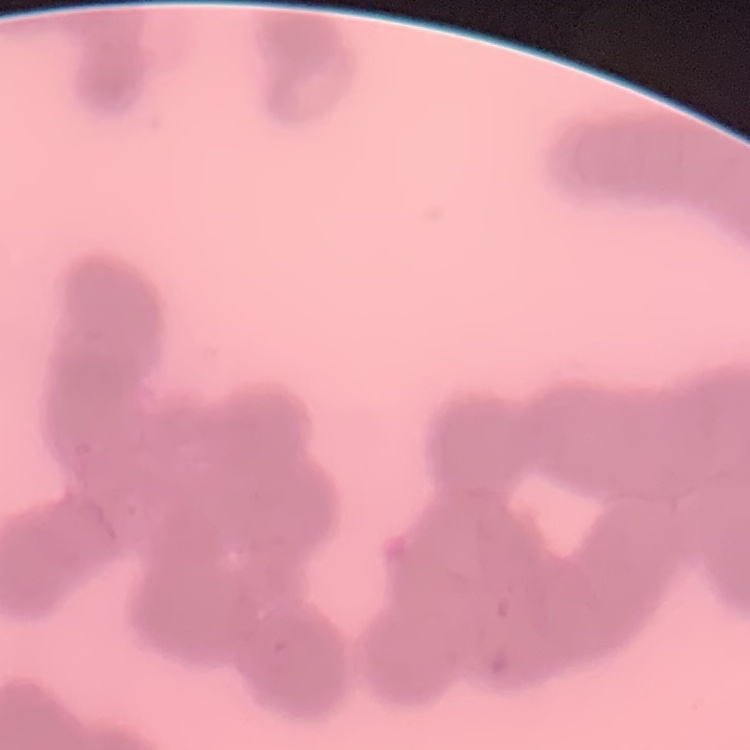

The red blood cells exhibit rouleaux formation. Thin blood smear. Stained with either Field's or Giemsa. Square crop of a larger photomicrograph.